Comment on the morphology of the erythrocytes.
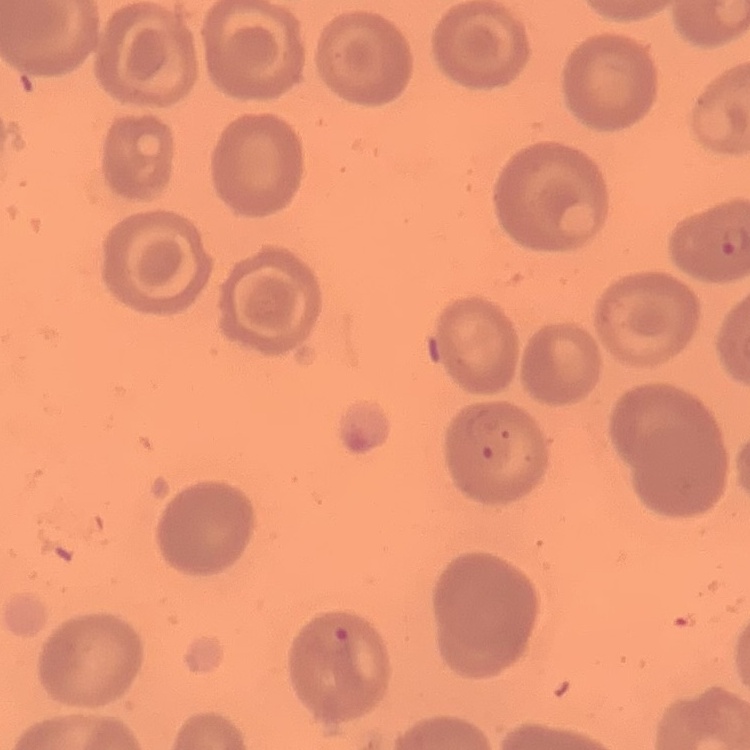
They show no rouleaux formation.

Field's or Giemsa stain. Square crop of a larger photomicrograph. Thin blood film.